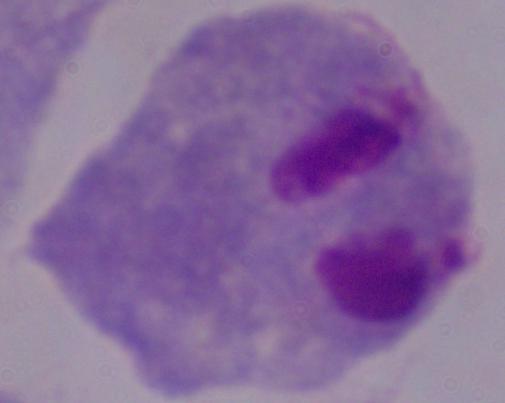

Summary:
  - Magnification: 1000x
  - Modality: micrograph
  - Identification: trichomonad